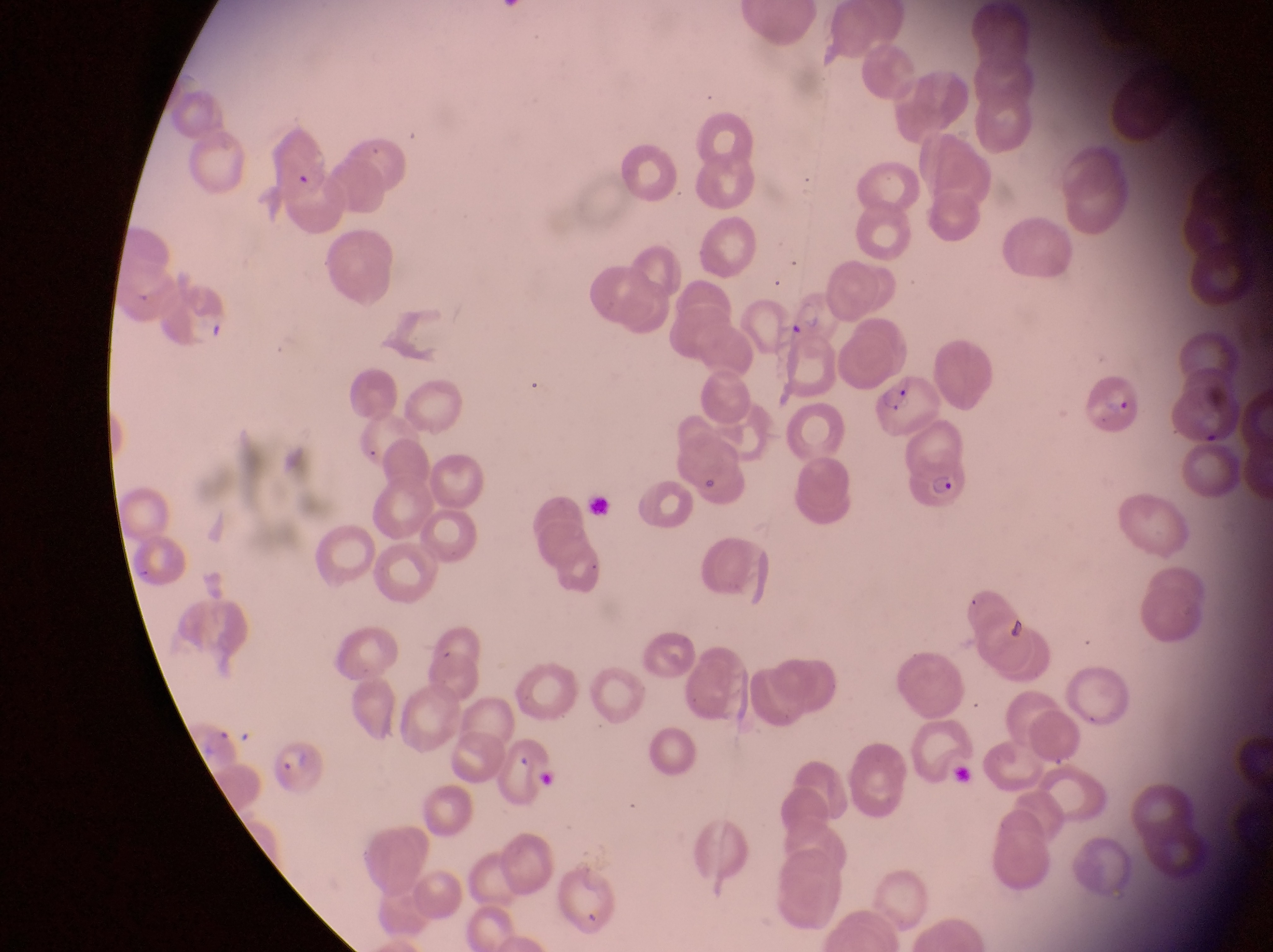

Approximate bounding boxes as left top right bottom in pixels.
Summary:
  - Parasitised red blood cell locations: 741 296 802 342; 1081 369 1139 435; 873 375 947 437; 906 455 975 510; 270 741 332 799
  - Field of view: single
  - Preparation: thin blood film
  - Country: Uganda
  - Capture: smartphone photograph through the eyepiece of an Olympus CX-23 microscope
  - Magnification: 1000x
  - Image size: 1273×952 pixels